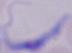 Micrograph. 1000x magnification. A trypanosome is shown.